Report the malaria status of this cell.
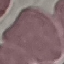
It is uninfected.

Automatically extracted cell patch, resized to 64 × 64 pixels. Thin blood smear. Giemsa-stained preparation. Photographed with a smartphone camera at the microscope eyepiece.